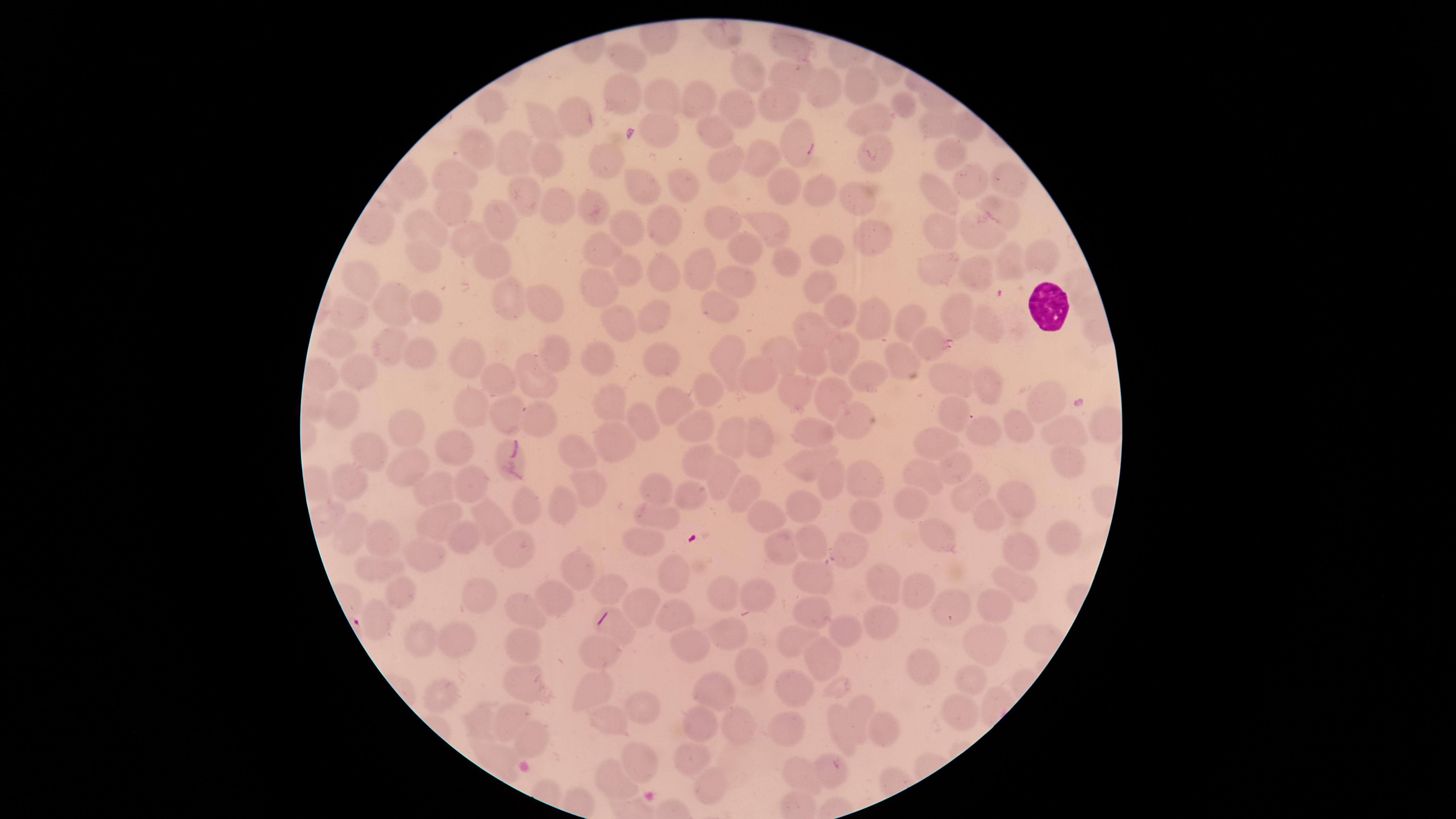 Approximate marker points as {x, y} in pixels. Uninfected red blood cells: {791, 42}, {631, 59}, {750, 74}, {791, 79}, {864, 84}, {827, 86}, {624, 90}, {665, 95}, {781, 102}, {696, 103}, {902, 106}, {498, 109}, {744, 110}, {577, 116}, {542, 118}, {869, 120}, {932, 125}, {708, 128}, {657, 133}, {796, 142}, {475, 145}, {510, 149}, {878, 151}, {943, 153}, {762, 156}, {609, 158}, {551, 162}, {720, 167}, {457, 173}, {412, 177}, {973, 178}, {1014, 179}, {683, 185}, {784, 185}, {641, 186}, {811, 189}, {523, 193}, {939, 193}, {857, 195}, {559, 202}, {454, 205}, {596, 205}, {1005, 211}, {375, 221}, {661, 222}, {717, 224}, {774, 224}, {507, 225}, {940, 226}, {427, 228}, {628, 229}, {983, 233}, {871, 234}, {470, 238}, {606, 245}, {742, 247}, {828, 250}, {1039, 255}, {494, 258}, {426, 259}, {785, 262}, {1011, 264}, {701, 267}, {934, 267}, {659, 271}, {627, 273}, {975, 275}, {364, 281}, {1076, 282}, {606, 283}, {736, 283}, {815, 285}, {389, 301}, {546, 302}, {514, 303}, {1081, 304}, {724, 305}, {840, 305}, {427, 306}, {354, 311}, {656, 314}, {868, 317}, {958, 317}, {907, 323}, {990, 324}, {618, 326}, {816, 328}, {333, 341}, {932, 344}, {390, 352}, {553, 352}, {840, 352}, {417, 356}, {777, 356}, {470, 357}, {663, 357}, {599, 360}, {816, 361}, {725, 362}, {907, 364}, {354, 371}, {759, 373}, {322, 375}, {877, 376}, {950, 377}, {497, 379}, {534, 379}, {987, 384}, {711, 385}, {793, 393}, {836, 397}, {1049, 401}, {666, 402}, {608, 403}, {470, 407}, {536, 414}, {344, 415}, {949, 416}, {510, 417}, {641, 417}, {1102, 421}, {856, 423}, {408, 426}, {983, 427}, {700, 428}, {1019, 429}, {1065, 431}, {813, 433}, {727, 434}, {759, 435}, {937, 439}, {617, 442}, {455, 444}, {373, 447}, {575, 453}, {1062, 456}, {698, 462}, {409, 463}, {802, 463}, {955, 463}, {868, 476}, {919, 476}, {713, 477}, {835, 477}, {342, 479}, {470, 481}, {656, 483}, {430, 484}, {587, 489}, {743, 490}, {974, 492}, {694, 497}, {1015, 499}, {529, 505}, {560, 505}, {918, 506}, {805, 508}, {765, 510}, {983, 512}, {865, 513}, {655, 516}, {490, 518}, {439, 519}, {351, 532}, {945, 532}, {1066, 533}, {809, 535}, {381, 540}, {464, 541}, {517, 543}, {641, 543}, {850, 543}, {784, 545}, {1019, 545}, {426, 555}, {370, 567}, {580, 567}, {673, 570}, {814, 577}, {884, 584}, {1017, 584}, {605, 592}, {401, 593}, {723, 593}, {920, 593}, {761, 594}, {472, 596}, {556, 600}, {639, 606}, {948, 607}, {987, 607}, {521, 610}, {812, 611}, {674, 613}, {375, 617}, {884, 621}, {850, 626}, {619, 629}, {725, 630}, {420, 637}, {792, 638}, {1047, 638}, {453, 639}, {977, 641}, {694, 648}, {521, 650}, {598, 652}, {825, 659}, {752, 665}, {925, 669}, {525, 679}, {972, 682}, {795, 686}, {596, 687}, {715, 690}, {443, 692}, {644, 706}, {858, 707}, {965, 713}, {608, 718}, {477, 719}, {511, 719}, {702, 725}, {736, 725}, {788, 726}, {884, 728}, {843, 730}, {532, 738}, {694, 756}, {642, 760}, {834, 769}, {800, 776}, {709, 780}, {620, 781}. White blood cells: {1042, 302}. Image is 1456×819 pixels. Thin smear of blood. Presence: no malaria parasites detected. The visible region is circular. Giemsa stain. Smartphone photograph through the microscope eyepiece. One field of view of the specimen.